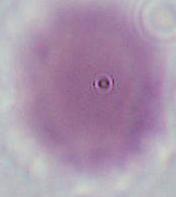
modality = micrograph
identification = red blood cell
magnification = 1000x